Report the malaria status of this cell.
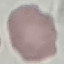
It is uninfected.

{
  "capture": "smartphone through the microscope eyepiece",
  "preparation": "thin blood film",
  "image_type": "automatically extracted cell patch, resized to 64 × 64 pixels",
  "stain": "Giemsa"
}